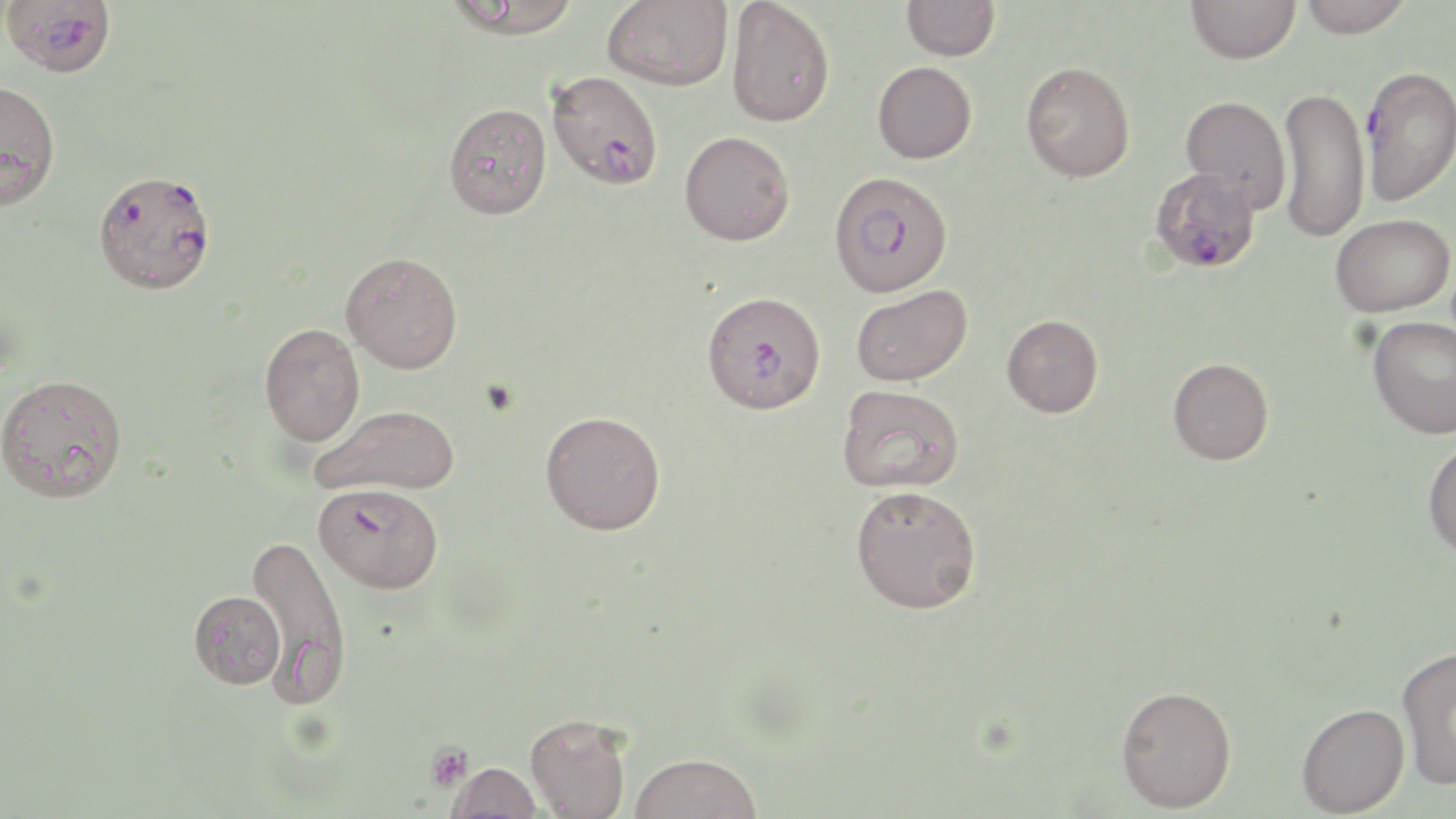

Approximate bounding boxes as (x1, y1, x2, y2) in pixels. Uninfected red blood cell locations: (444, 0, 583, 38), (603, 0, 733, 90), (725, 0, 835, 127), (901, 0, 999, 61), (1186, 0, 1300, 63), (1299, 0, 1412, 39), (873, 61, 977, 163), (1021, 61, 1135, 182), (0, 80, 61, 210), (1277, 86, 1369, 242), (1179, 95, 1292, 212), (444, 103, 552, 219), (680, 130, 795, 245), (1330, 214, 1454, 316), (341, 251, 463, 373), (850, 284, 972, 386), (1001, 315, 1103, 418), (1367, 316, 1456, 438), (259, 322, 366, 446), (1168, 357, 1273, 465), (0, 373, 128, 503), (837, 384, 964, 493), (310, 404, 461, 497), (540, 410, 666, 534), (1422, 437, 1456, 558), (850, 485, 982, 614), (246, 533, 352, 703), (189, 590, 285, 689), (1396, 645, 1456, 790), (1115, 685, 1237, 812), (1296, 703, 1409, 817), (525, 713, 631, 819), (629, 752, 763, 819), (446, 761, 542, 819). Platelet locations: (426, 742, 472, 791). Plasmodium falciparum-infected red blood cell locations: (2, 1, 115, 78), (1360, 65, 1456, 205), (546, 71, 664, 191), (1148, 165, 1261, 274), (828, 170, 953, 298), (95, 175, 213, 302), (701, 290, 826, 414), (313, 481, 444, 594). Slide-level diagnosis: Plasmodium falciparum. May-Grünwald-Giemsa-stained preparation. 1000x magnification. One field of a larger specimen. Image is 1456×819 pixels. Thin blood film. Optical microscopy.